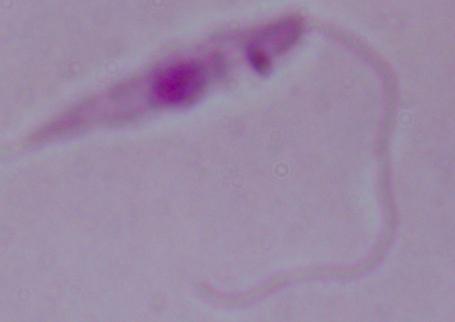 Captured at 1000x magnification. A Leishmania parasite is seen. Photomicrograph.